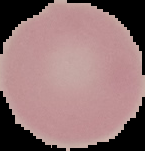

Result: no malaria parasites seen. Image is 145×151 pixels. From a thin blood smear. Segmented cell region on a black background.